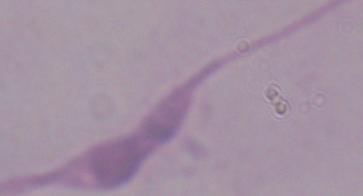
Photomicrograph. A Leishmania parasite is shown. Captured at 1000x magnification.